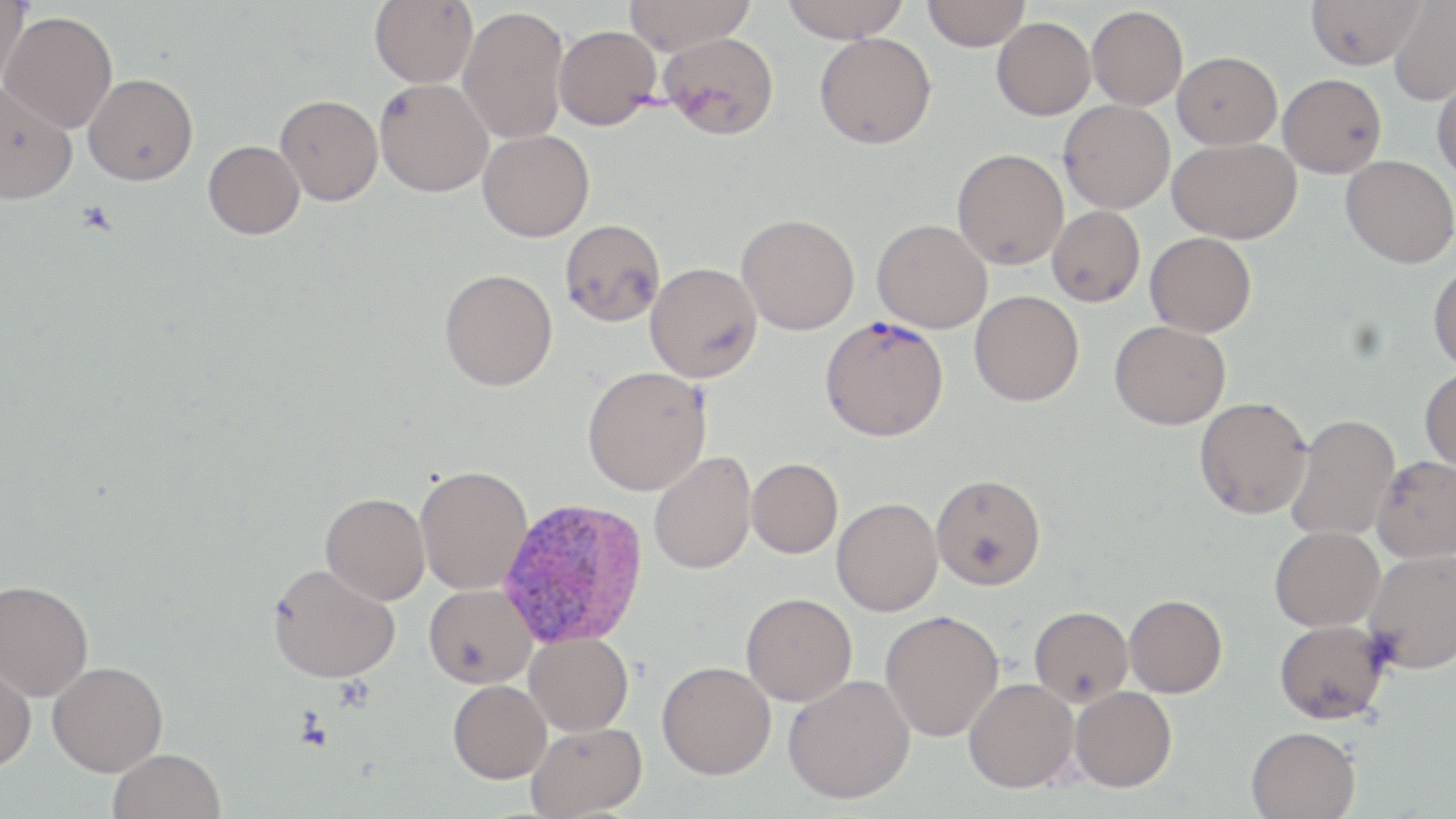

Summary:
  - Coordinate format: approximate bounding boxes as [x1, y1, x2, y2] in pixels
  - Plasmodium vivax-infected red blood cell locations: [497, 498, 649, 649]
  - Platelet locations: [76, 201, 118, 237]
  - Uninfected red blood cell locations: [369, 0, 478, 88], [623, 0, 755, 55], [780, 0, 911, 42], [923, 0, 1030, 51], [1305, 0, 1424, 69], [0, 1, 30, 92], [1389, 1, 1456, 105], [1087, 5, 1188, 109], [458, 6, 569, 144], [1, 10, 118, 133], [992, 17, 1095, 120], [554, 24, 661, 129], [659, 31, 780, 139], [814, 32, 936, 149], [1172, 51, 1281, 149], [1432, 72, 1456, 184], [83, 73, 198, 185], [1278, 73, 1387, 177], [374, 78, 493, 197], [0, 81, 77, 204], [274, 94, 383, 206], [1058, 100, 1175, 213], [478, 130, 594, 242], [1167, 137, 1300, 243], [203, 140, 305, 239], [952, 149, 1068, 270], [1341, 155, 1456, 268], [1047, 206, 1145, 306], [736, 213, 859, 335], [559, 219, 665, 326], [872, 219, 992, 333], [1145, 232, 1257, 336], [1427, 261, 1456, 373], [645, 262, 762, 382], [439, 268, 558, 391], [969, 290, 1083, 406], [820, 315, 949, 441], [1109, 320, 1230, 429], [582, 366, 711, 495], [1419, 368, 1456, 473], [1194, 397, 1312, 519], [1285, 414, 1401, 542], [649, 452, 756, 574], [1371, 454, 1456, 564], [747, 457, 843, 557], [415, 464, 533, 595], [930, 472, 1046, 590], [320, 492, 430, 604], [832, 497, 942, 616], [1270, 525, 1385, 631], [1363, 548, 1456, 674], [267, 562, 400, 682], [0, 580, 94, 700], [423, 584, 536, 688], [741, 592, 858, 706], [1124, 594, 1228, 697], [1029, 605, 1133, 706], [879, 609, 1004, 741], [1273, 619, 1389, 724], [524, 631, 633, 736], [0, 654, 37, 772], [47, 661, 168, 775], [657, 661, 776, 779], [783, 674, 915, 803], [963, 677, 1079, 793], [448, 680, 551, 783], [1070, 686, 1176, 791], [526, 722, 648, 818], [1246, 726, 1361, 819], [108, 748, 225, 819]
  - Slide-level diagnosis: Plasmodium vivax
  - Field of view: one of a larger specimen
  - Image size: 1456×819 pixels
  - Stain: May-Grünwald-Giemsa
  - Modality: light microscopy
  - Magnification: 1000x
  - Preparation: thin blood smear